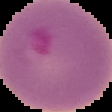

result = malaria parasites identified
preparation = thin blood film
image type = cell region segmented out of the field of view; surrounding area masked to black
image size = 112×112 pixels